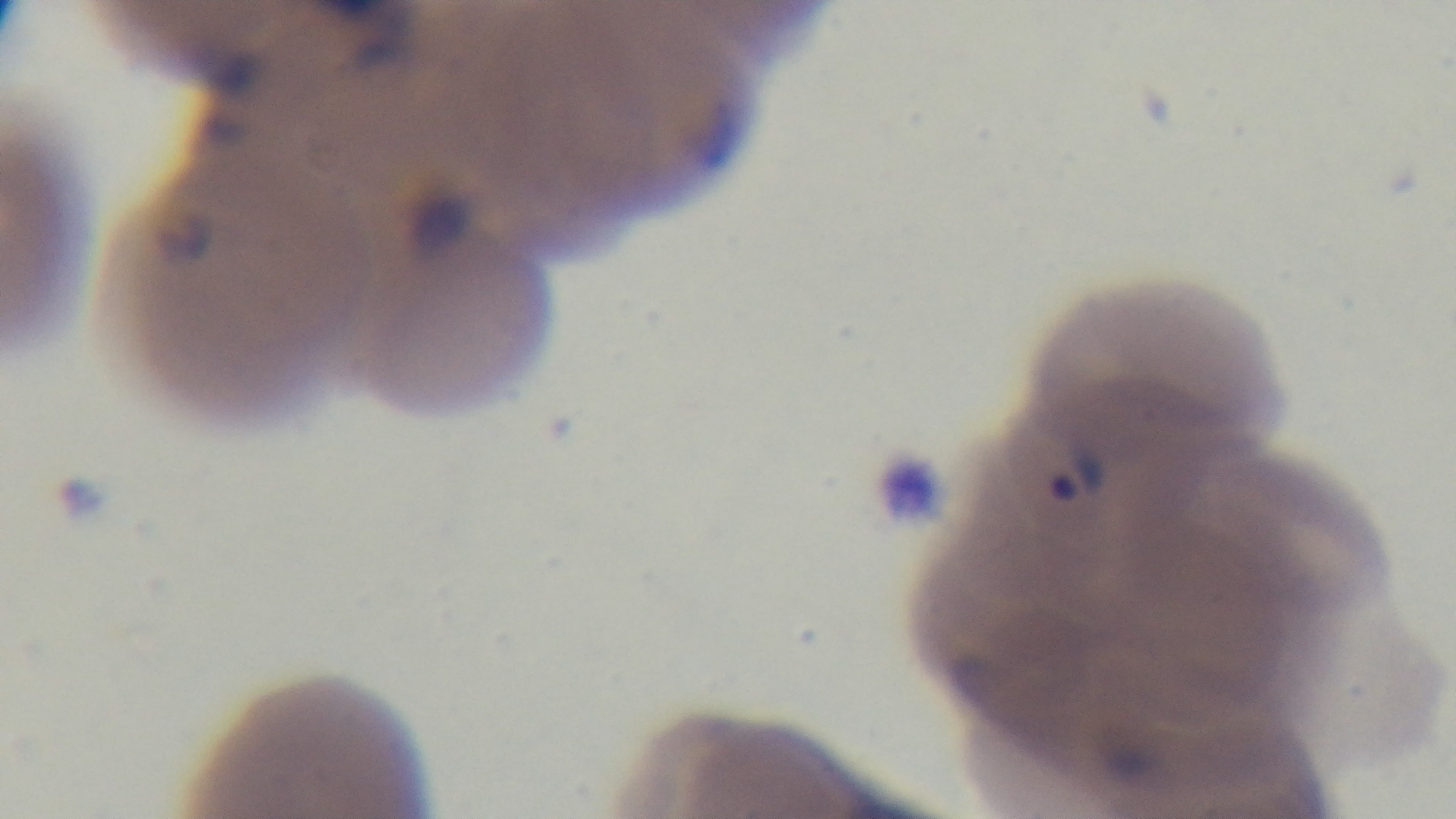

Light microscopy. One field from the slide. Mounted 4K digital camera. Giemsa-stained. Preparation: thin blood film. Malaria status: positive. 100x oil-immersion objective.